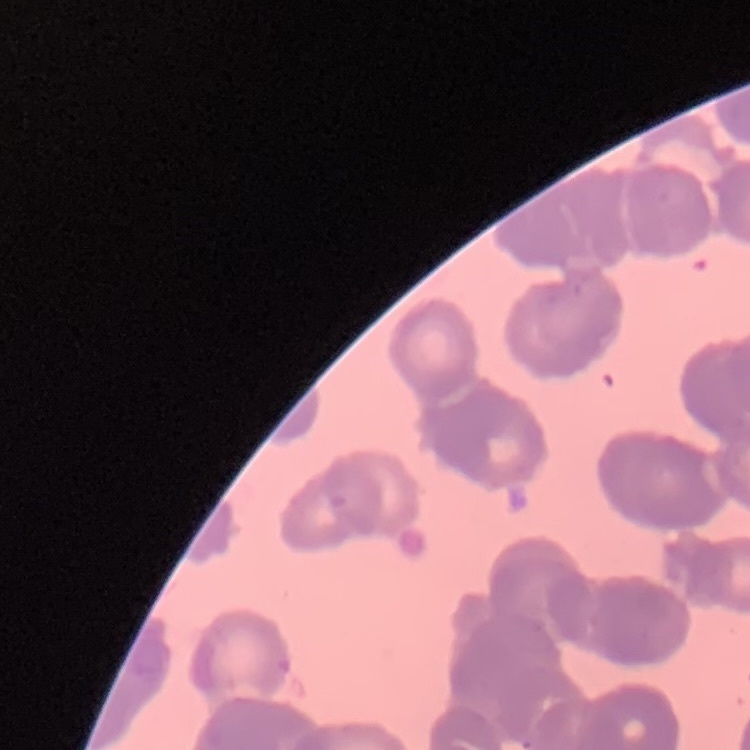

red blood cell morphology = rouleaux formation
stain = Field's or Giemsa
image type = one tile cut from a larger photomicrograph
preparation = thin peripheral smear